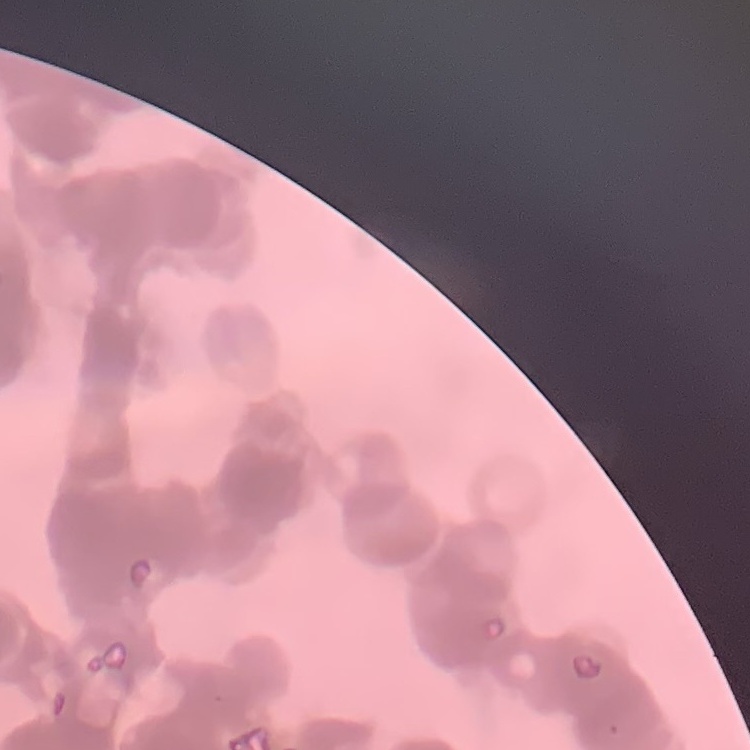

red blood cell morphology = rouleaux formation
image type = one tile cut from a larger photomicrograph
preparation = thin peripheral smear
stain = Field's or Giemsa